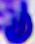

Summary:
  - Modality: micrograph
  - Magnification: 400x
  - Identification: leukocyte